Locate every malaria parasite.
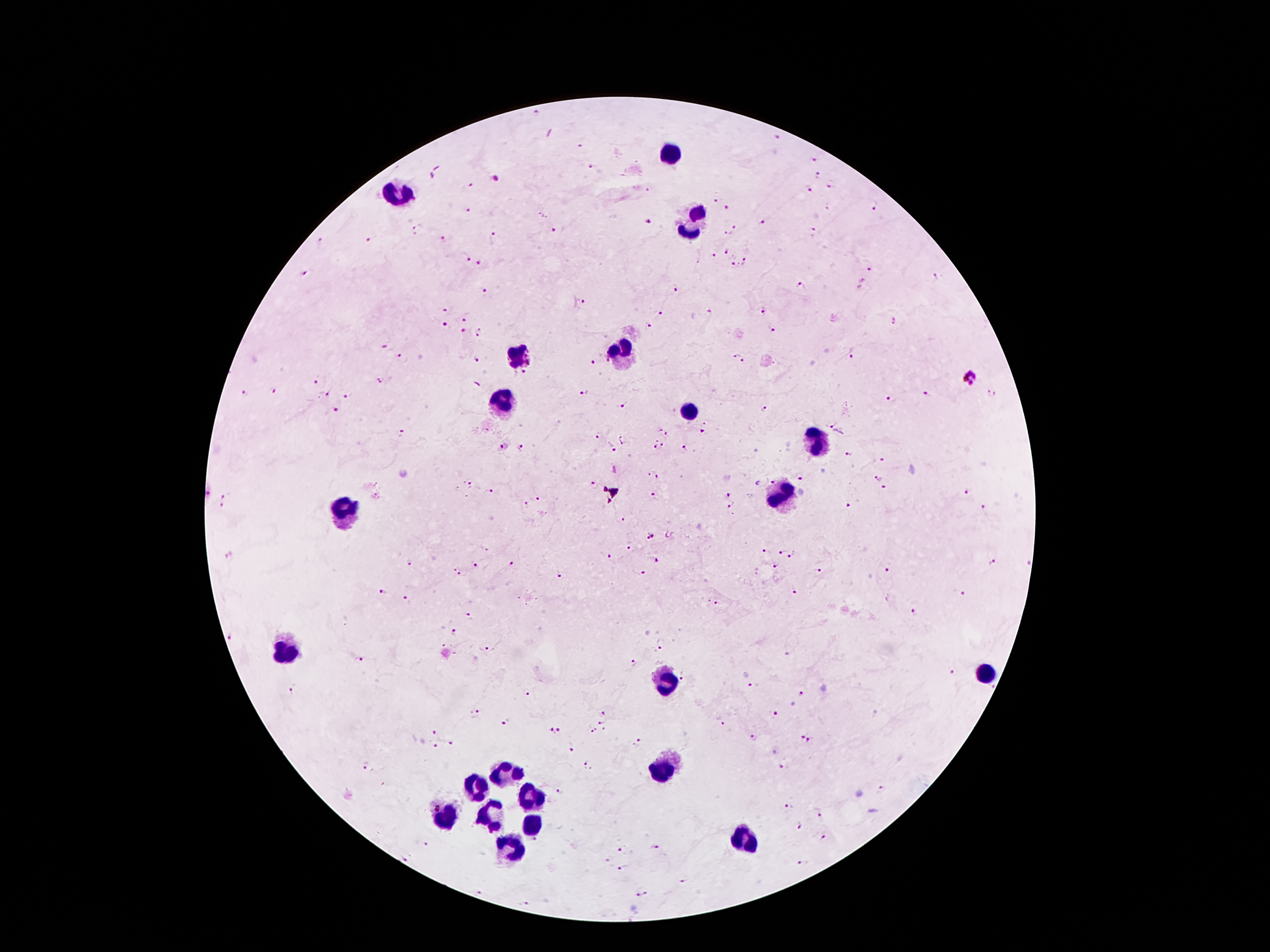
Approximate object centers, in pixels from the top-left corner.
Malaria parasites: (x=536, y=112), (x=777, y=137), (x=578, y=145), (x=812, y=160), (x=592, y=167), (x=819, y=176), (x=495, y=179), (x=471, y=186), (x=830, y=187), (x=808, y=188), (x=648, y=190), (x=714, y=201), (x=874, y=205), (x=725, y=208), (x=468, y=212), (x=763, y=219), (x=648, y=223), (x=735, y=228), (x=416, y=230), (x=555, y=230), (x=814, y=230), (x=726, y=234), (x=495, y=237), (x=321, y=240), (x=370, y=240), (x=443, y=240), (x=725, y=254), (x=713, y=255), (x=465, y=259), (x=745, y=261), (x=478, y=262), (x=735, y=266), (x=871, y=269), (x=305, y=274), (x=935, y=275), (x=800, y=284), (x=674, y=289), (x=484, y=291), (x=583, y=302), (x=445, y=308), (x=764, y=312), (x=658, y=313), (x=466, y=319), (x=896, y=321), (x=648, y=325), (x=445, y=326), (x=771, y=329), (x=465, y=332), (x=478, y=334), (x=384, y=346), (x=851, y=354), (x=735, y=355), (x=400, y=357), (x=477, y=360), (x=742, y=362), (x=593, y=363), (x=525, y=373), (x=970, y=377), (x=381, y=379), (x=316, y=381), (x=276, y=390), (x=992, y=392), (x=585, y=393), (x=926, y=393), (x=246, y=394), (x=330, y=394), (x=349, y=394), (x=891, y=399), (x=621, y=406), (x=765, y=410), (x=335, y=413), (x=831, y=424), (x=701, y=431), (x=400, y=433), (x=663, y=433), (x=597, y=437), (x=624, y=440), (x=663, y=445), (x=653, y=446), (x=521, y=448), (x=612, y=448), (x=684, y=448), (x=503, y=449), (x=849, y=452), (x=882, y=461), (x=653, y=475), (x=879, y=478), (x=801, y=479), (x=771, y=480), (x=470, y=484), (x=595, y=485), (x=883, y=489), (x=489, y=491), (x=966, y=491), (x=652, y=496), (x=729, y=496), (x=225, y=498), (x=537, y=500), (x=224, y=505), (x=525, y=505), (x=729, y=508), (x=849, y=508), (x=983, y=508), (x=624, y=519), (x=670, y=534), (x=649, y=537), (x=630, y=547), (x=765, y=551), (x=783, y=553), (x=231, y=555), (x=794, y=556), (x=612, y=558), (x=655, y=560), (x=514, y=562), (x=991, y=563), (x=1028, y=563), (x=410, y=564), (x=475, y=566), (x=775, y=567), (x=820, y=569), (x=887, y=570), (x=457, y=572), (x=640, y=573), (x=559, y=574), (x=795, y=592), (x=382, y=593), (x=962, y=594), (x=405, y=598), (x=718, y=604), (x=914, y=612), (x=469, y=616), (x=455, y=634), (x=231, y=637), (x=661, y=648), (x=483, y=650), (x=788, y=652), (x=359, y=659), (x=633, y=665), (x=953, y=673), (x=683, y=676), (x=751, y=685), (x=291, y=691), (x=527, y=694), (x=801, y=694), (x=475, y=714), (x=604, y=714), (x=775, y=715), (x=507, y=722), (x=600, y=723), (x=723, y=724), (x=592, y=730), (x=603, y=730), (x=434, y=732), (x=553, y=733), (x=800, y=734), (x=753, y=738), (x=811, y=741), (x=640, y=742), (x=451, y=743), (x=435, y=746), (x=571, y=749), (x=366, y=765), (x=588, y=766), (x=782, y=768), (x=882, y=789), (x=560, y=791), (x=789, y=805), (x=820, y=816), (x=799, y=826), (x=824, y=838), (x=424, y=845), (x=654, y=848), (x=622, y=851), (x=608, y=859), (x=406, y=860), (x=804, y=864), (x=621, y=869), (x=683, y=879), (x=481, y=893), (x=642, y=894), (x=525, y=904).

leukocyte locations = (x=670, y=155), (x=400, y=193), (x=693, y=221), (x=619, y=353), (x=519, y=356), (x=504, y=407), (x=688, y=414), (x=815, y=440), (x=781, y=496), (x=344, y=510), (x=285, y=649), (x=985, y=675), (x=669, y=680), (x=665, y=765), (x=501, y=775), (x=476, y=788), (x=532, y=797), (x=445, y=814), (x=492, y=817), (x=532, y=830), (x=741, y=840), (x=512, y=848)
magnification = 100x
stain = Giemsa
patient malaria status = infected with Plasmodium falciparum
field of view = one from this slide
preparation = thick blood film
capture = smartphone through the microscope eyepiece
image size = 1270×952 pixels